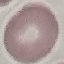
result = negative for malaria parasites
image type = cell patch, automatically extracted from a larger field of view and resized to 64 × 64 pixels
stain = Giemsa
preparation = thin blood film
capture = smartphone camera at the microscope eyepiece